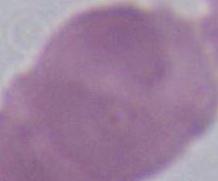

{
  "identification": "erythrocyte",
  "magnification": "1000x",
  "modality": "photomicrograph"
}